Assess for Plasmodium parasites.
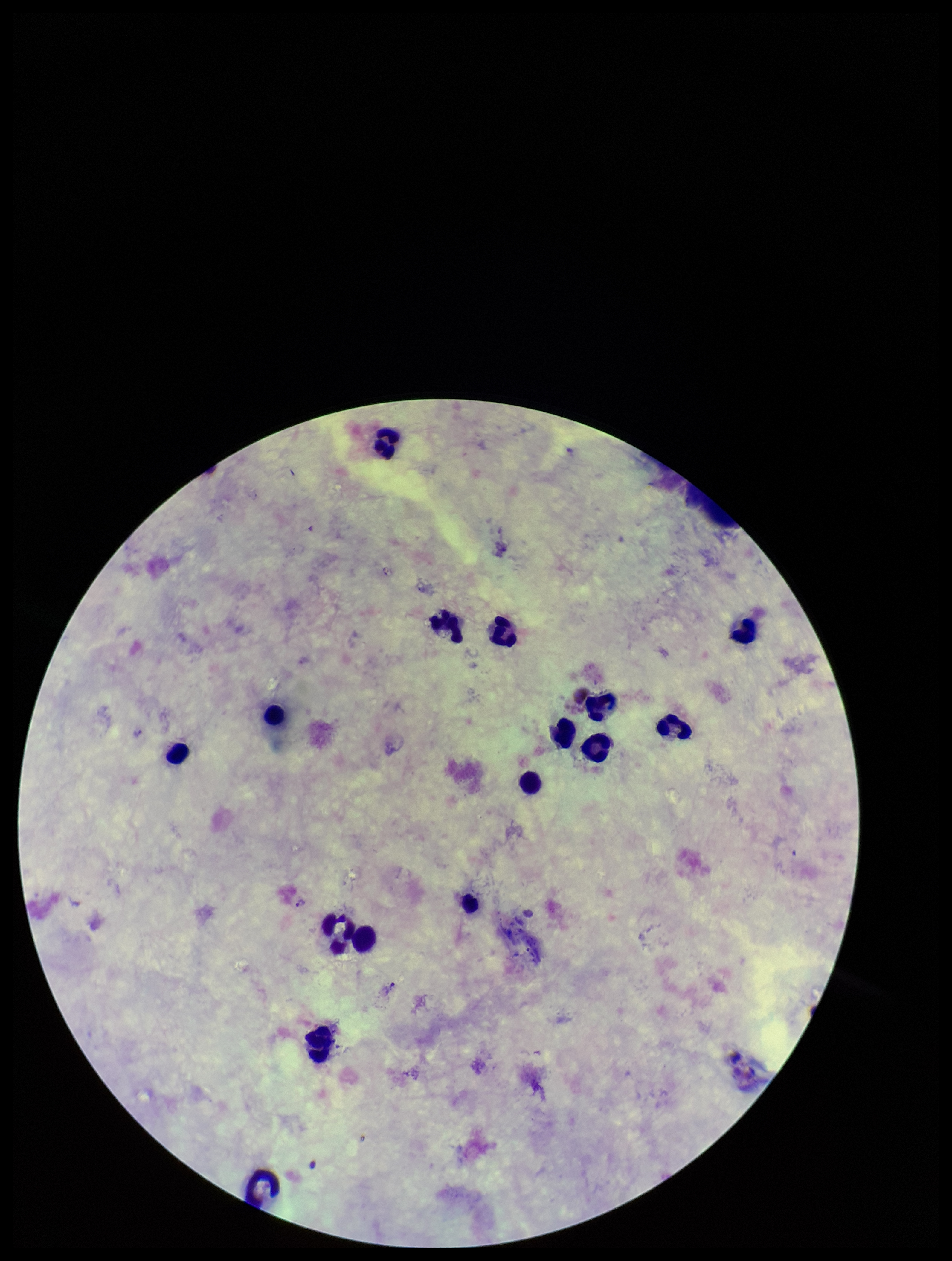

Detected.

Preparation: thick smear. Image is 952×1261 pixels. Leukocyte count: 16. Species reported for this patient: Plasmodium vivax. Giemsa stain. One field from this slide. Photographed through the microscope eyepiece with a smartphone camera. Patient malaria status: infected. Parasite count: 3.